Give the preparation type.
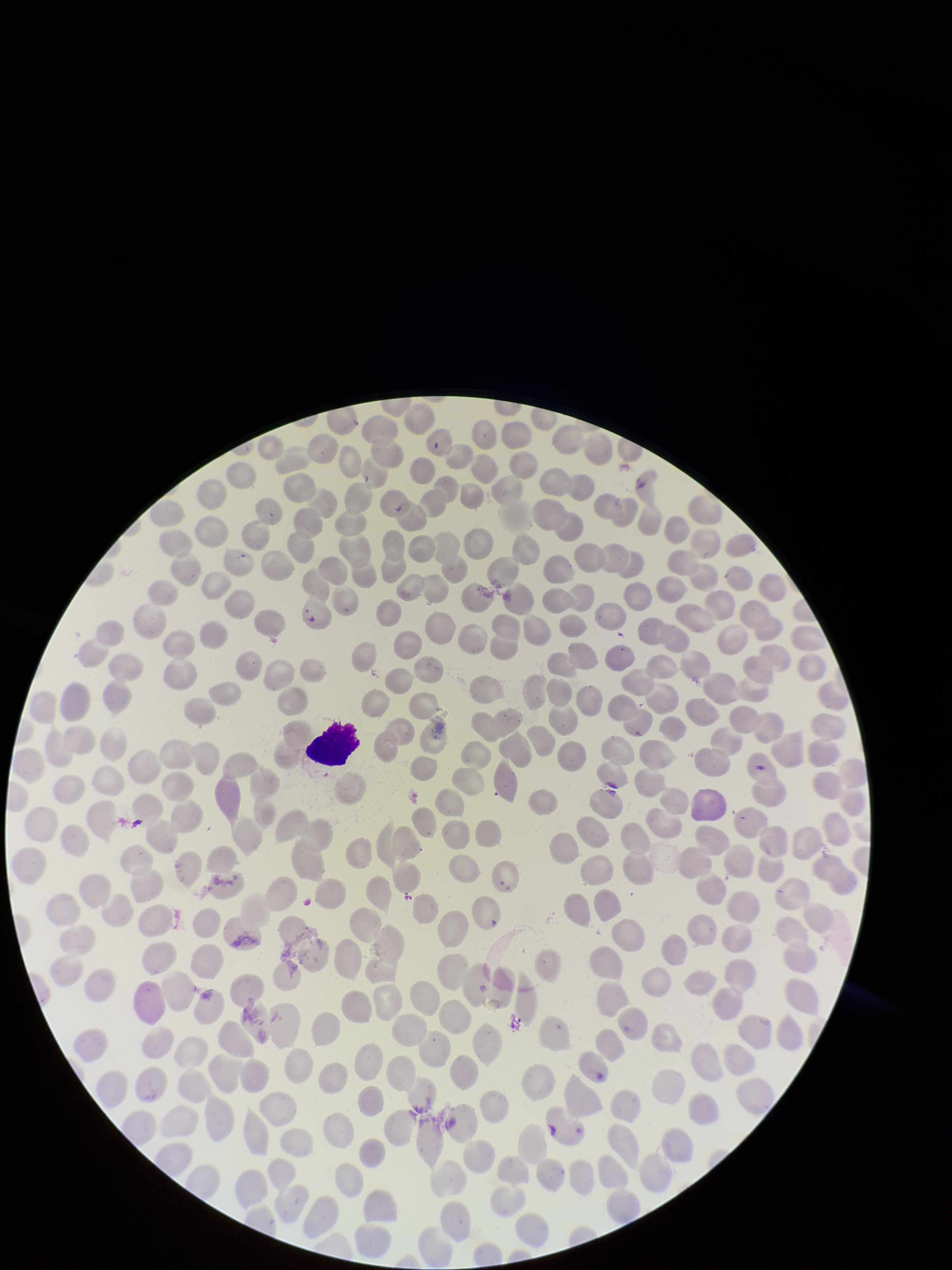

Thin.

{
  "stain": "Giemsa",
  "parasitized_red_blood_cells": "none seen",
  "patient_malaria_status": "negative",
  "parasitized_red_blood_cell_count": 0,
  "image_size": "952×1270 pixels",
  "capture": "smartphone photograph through the microscope eyepiece",
  "field_of_view": "one from this slide",
  "red_blood_cell_count": 320
}